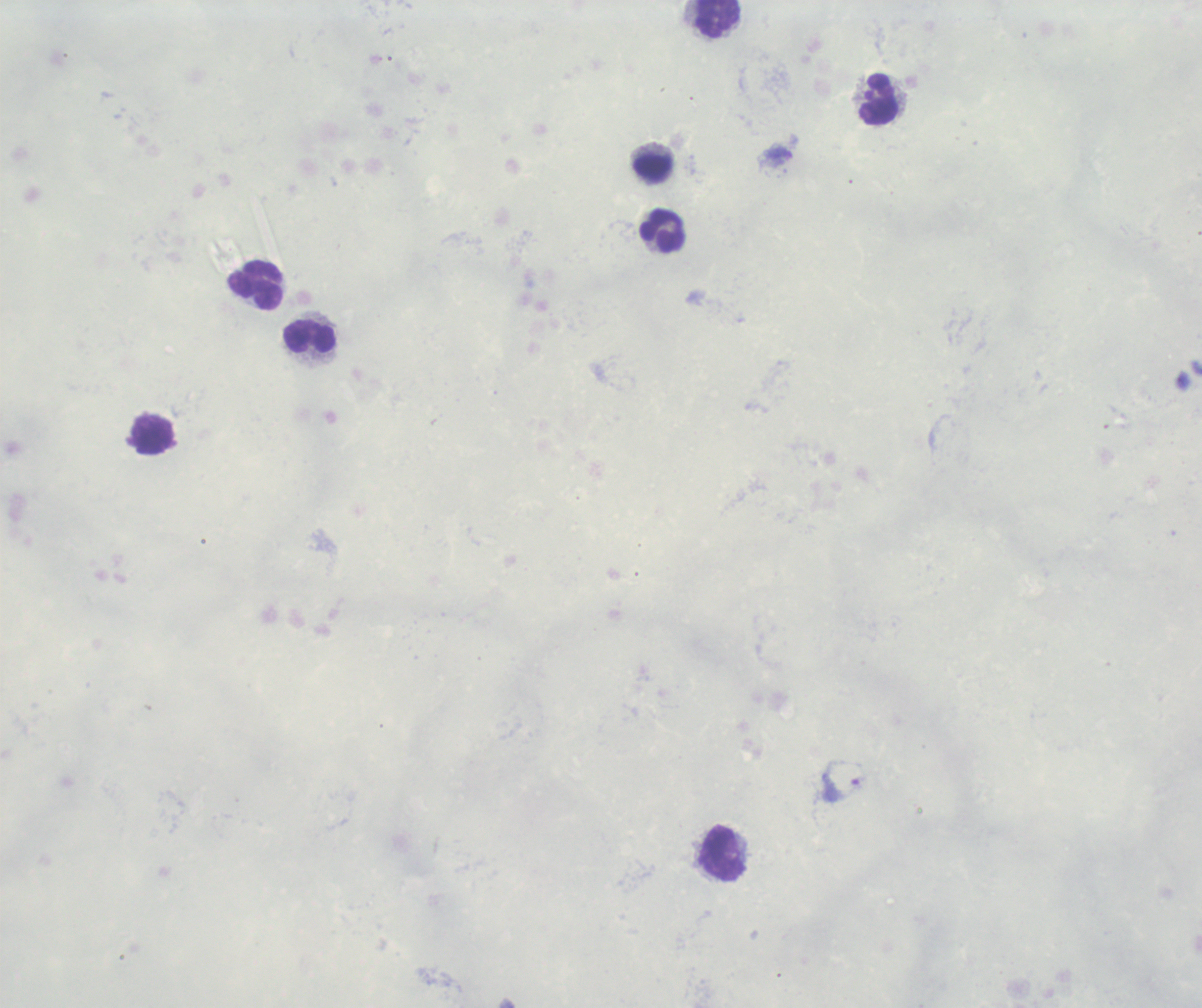
coordinate format = approximate object centers, in pixels from the top-left corner
trophozoite locations = (x=841, y=780)
leukocyte locations = (x=717, y=19), (x=879, y=99), (x=652, y=167), (x=662, y=231), (x=255, y=285), (x=310, y=337), (x=151, y=435), (x=724, y=854)
field of view = one from this slide
background quality = poor
image size = 1202×1008 pixels
preparation = thick blood smear
context = previously used in an actual diagnosis
stain = Romanowsky
result = positive for malaria parasites
magnification = 100x